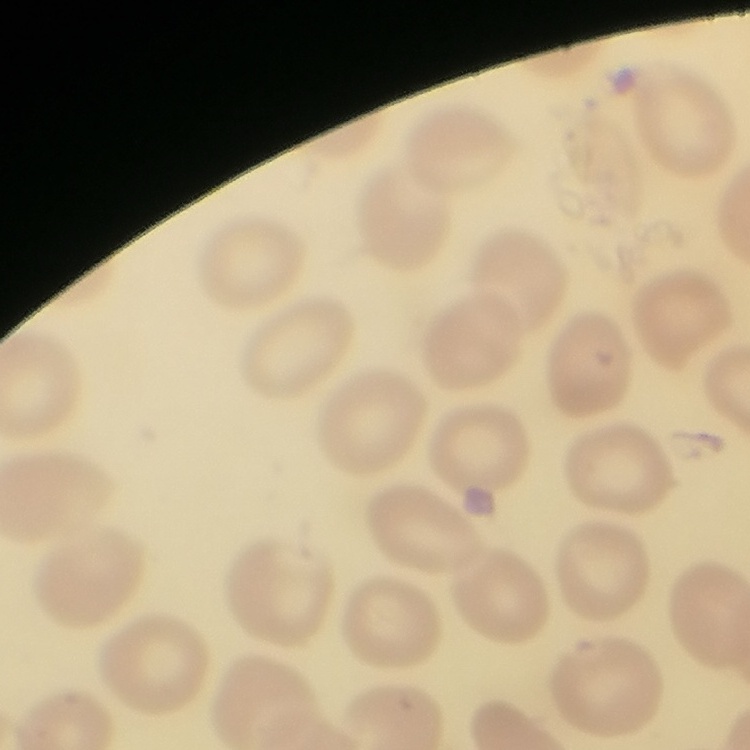

The red blood cells show no rouleaux formation. Stained with either Field's or Giemsa. Square crop of a larger photomicrograph. Thin blood smear.